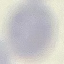

Result: no malaria parasites seen. Acquired by smartphone through the microscope eyepiece. Automatically extracted cell patch, resized to 64 × 64 pixels. Thin blood film. Giemsa stain.